Assess the morphology of the red blood cells.
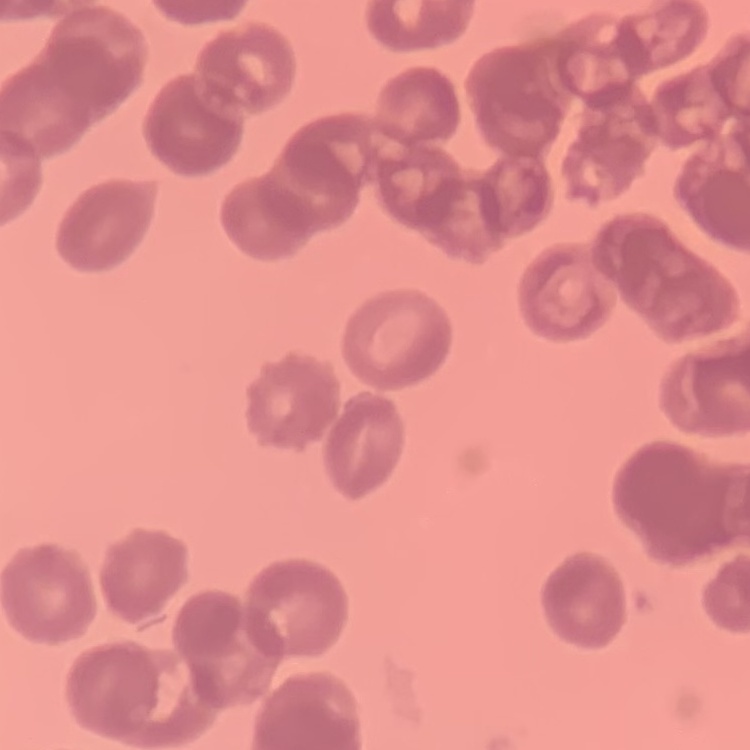

They show rouleaux formation.

Summary:
  - Stain: Field's or Giemsa
  - Preparation: thin blood smear
  - Image type: one tile cut from a larger photomicrograph